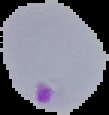

{
  "result": "Plasmodium parasites identified",
  "image_size": "109×115 pixels",
  "image_type": "segmented cell region with the area outside set to black",
  "preparation": "thin blood film"
}